State the preparation type.
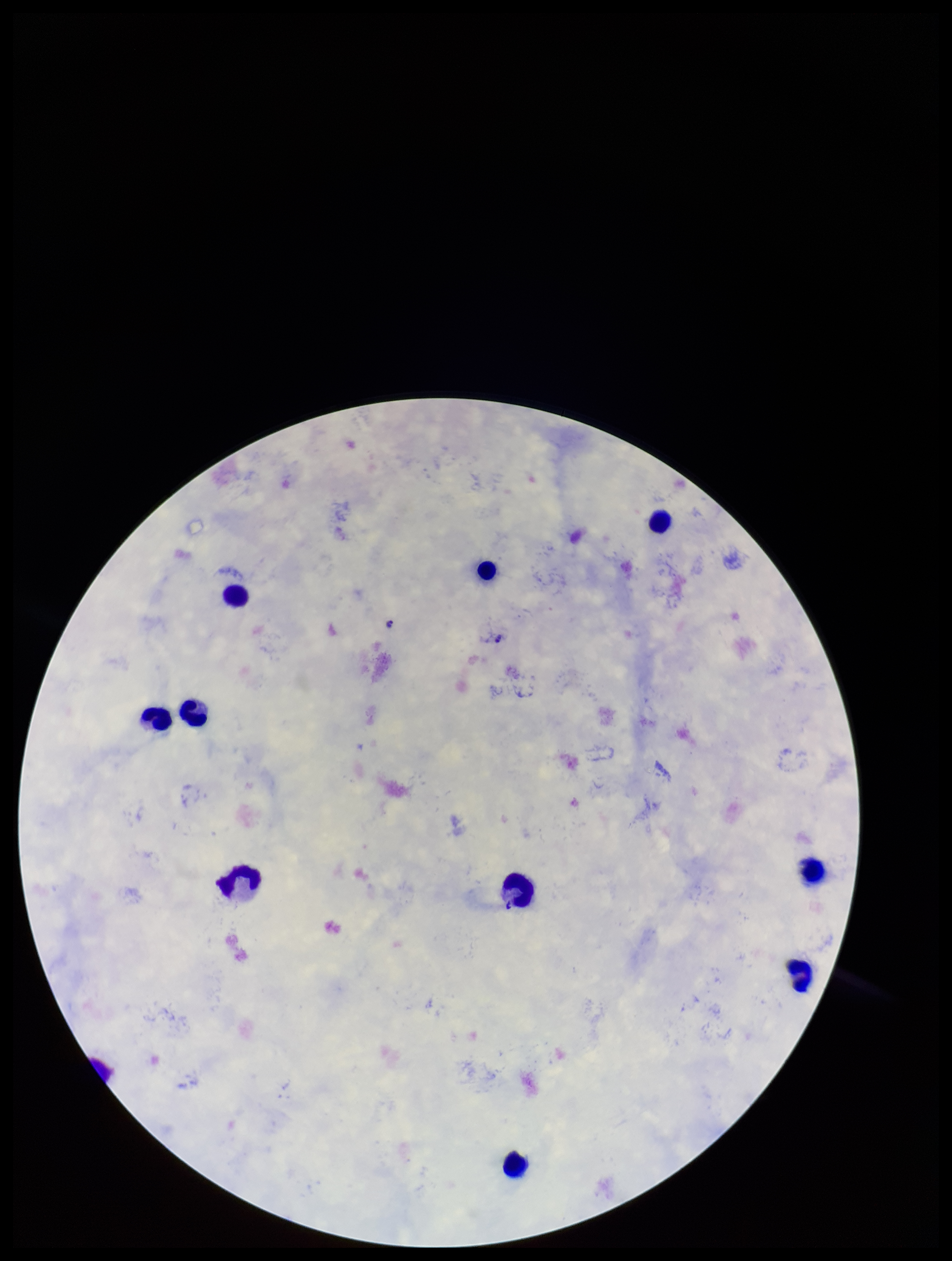
A thick smear.

Summary:
  - Stain: Giemsa
  - Capture: smartphone photograph through the microscope eyepiece
  - Image size: 952×1261 pixels
  - Patient malaria status: infected
  - Leukocyte count: 11
  - Parasite count: 0
  - Species reported for this patient: Plasmodium falciparum
  - Field of view: one from this slide
  - Plasmodium parasites: none detected